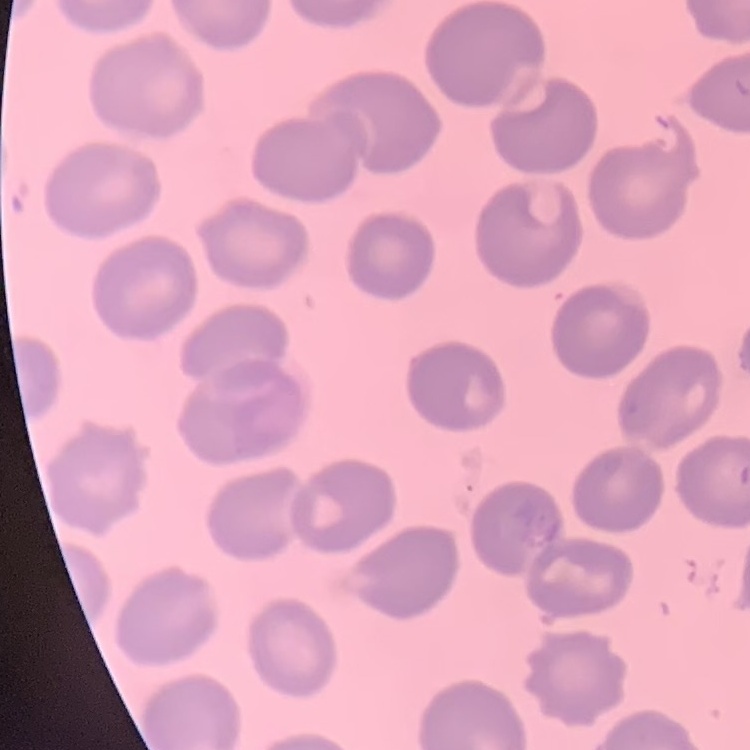

red blood cell morphology = no rouleaux formation
stain = Field's or Giemsa
preparation = thin blood film
image type = one tile cut from a larger photomicrograph